Comment on the morphology of the erythrocytes.
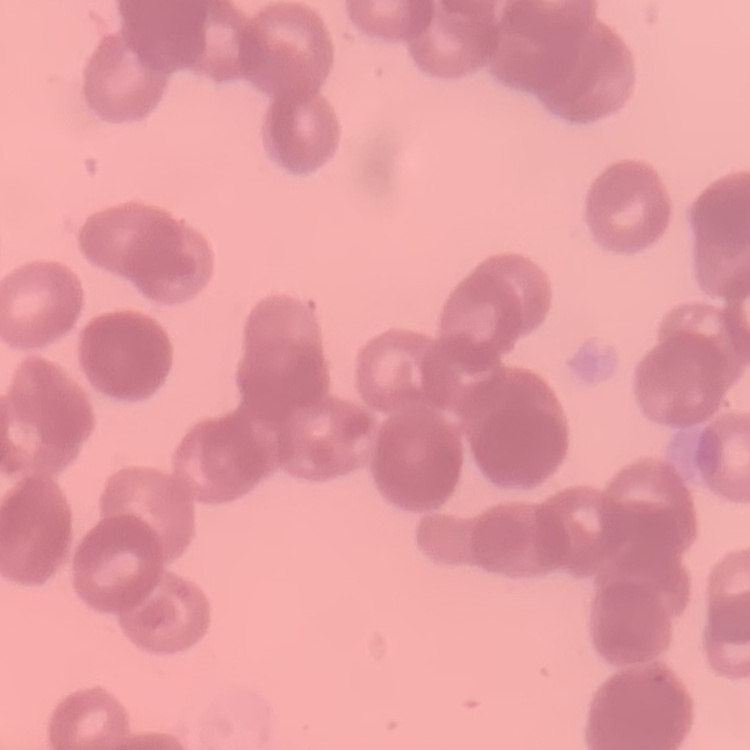
They show rouleaux formation.

stain = Field's or Giemsa
preparation = thin blood smear
image type = square crop of a larger photomicrograph